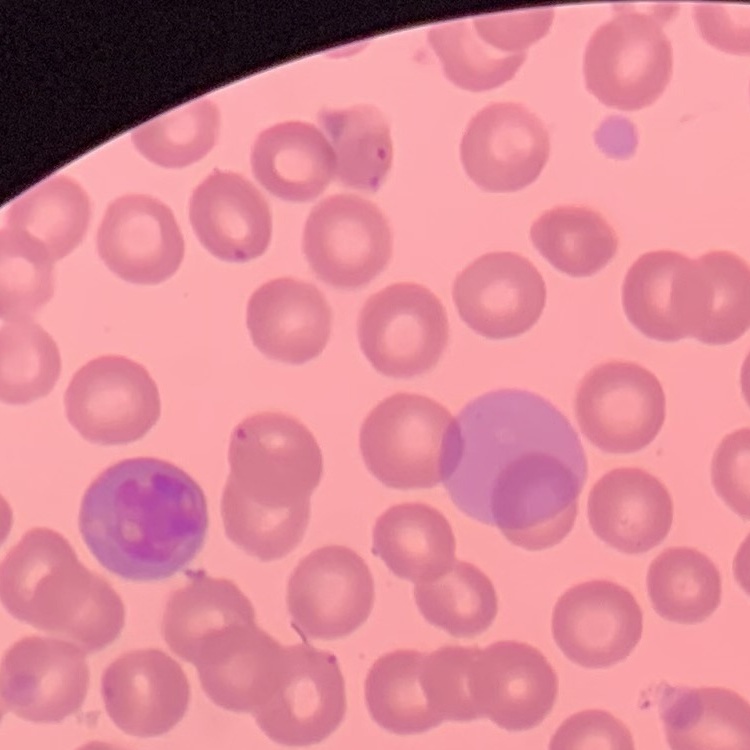
Summary:
  - Erythrocyte morphology: no rouleaux formation
  - Preparation: thin peripheral smear
  - Stain: Field's or Giemsa
  - Image type: square crop of a larger photomicrograph